Identify the cell.
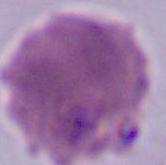
An erythrocyte.

Summary:
  - Modality: micrograph
  - Magnification: 1000x